Report the malaria status of this cell.
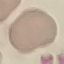

It is uninfected.

Summary:
  - Stain: Giemsa
  - Preparation: thin blood smear
  - Capture: smartphone through the microscope eyepiece
  - Image type: cell patch, automatically extracted from a larger field of view and resized to 64 × 64 pixels